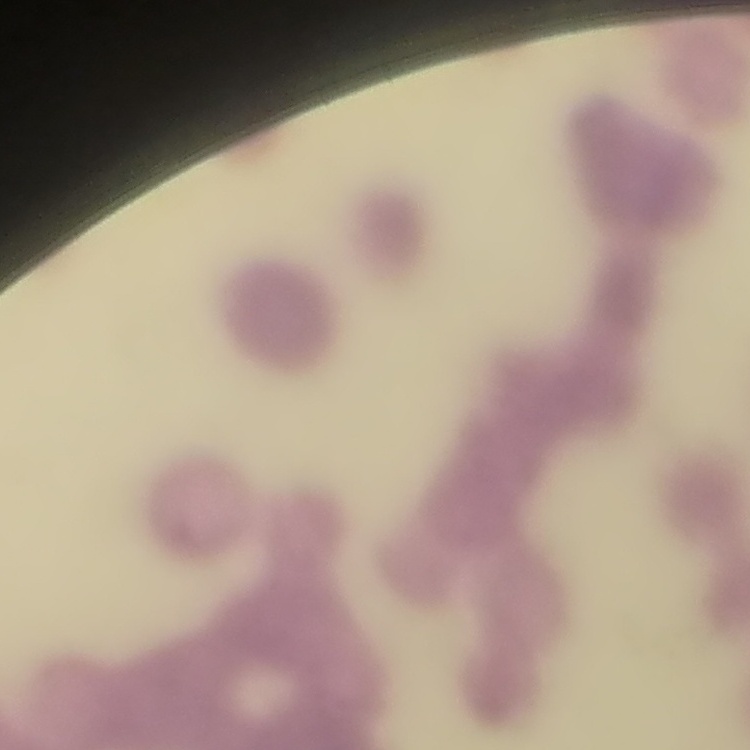

red blood cell morphology = rouleaux formation
stain = Field's or Giemsa
preparation = thin peripheral smear
image type = one tile cut from a larger photomicrograph